Identify the preparation type.
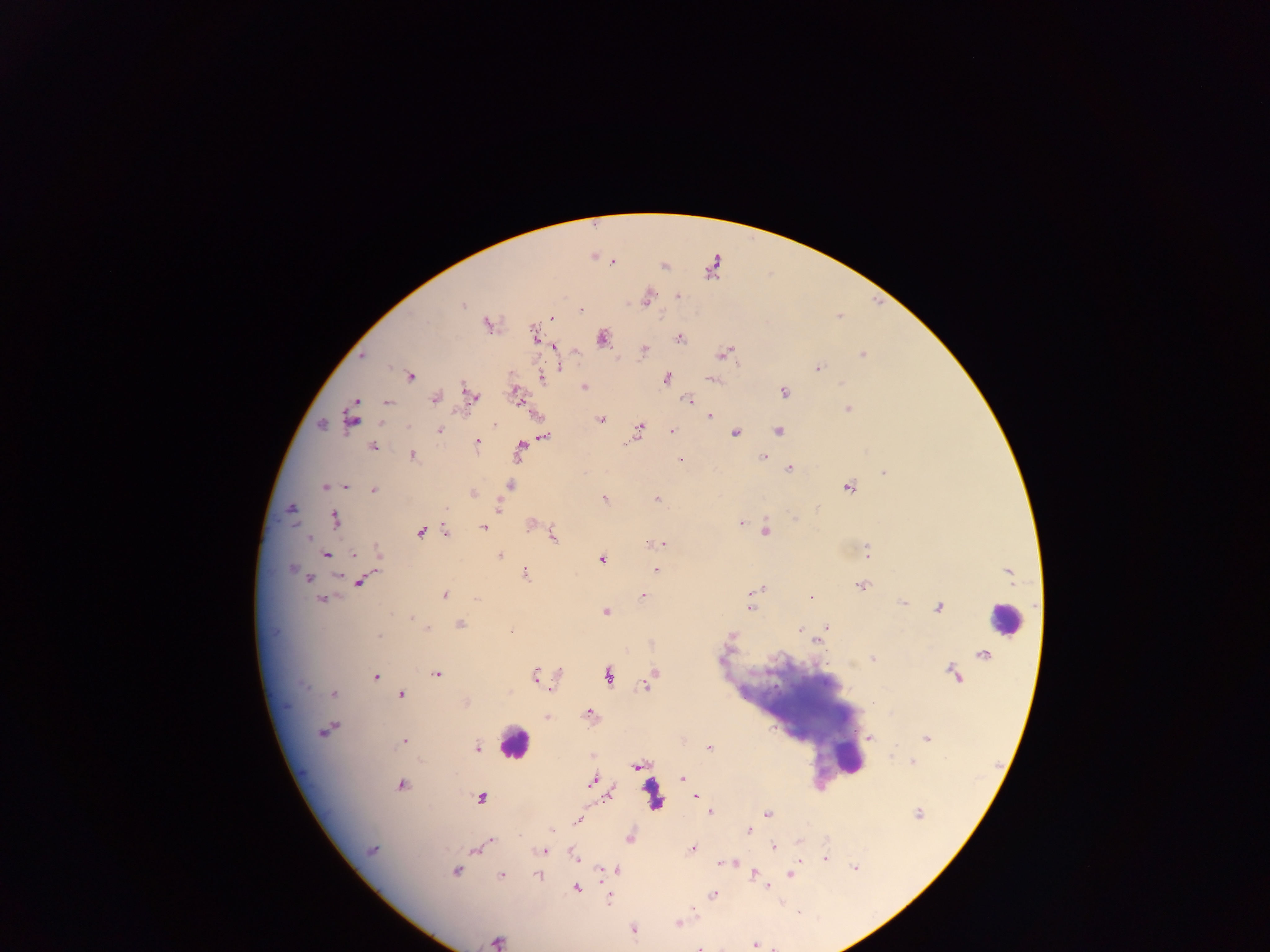
This is a thick smear.

capture = mobile-phone photograph through a microscope
leukocyte locations = approximate centers as [x, y] in pixels: [1004, 619], [513, 742], [849, 759], [652, 794]
image size = 1270×952 pixels
field of view = single
country = Ghana
malaria parasite locations = approximate centers as [x, y] in pixels: [592, 257], [613, 261], [664, 264], [677, 296], [647, 297], [462, 305], [581, 311], [551, 319], [488, 323], [534, 334], [603, 337], [679, 338], [554, 346], [644, 349], [724, 353], [862, 354], [362, 356], [560, 365], [817, 368], [409, 376], [540, 377], [666, 378], [712, 378], [584, 386], [783, 392], [515, 395], [472, 396], [434, 397], [687, 399], [519, 400], [355, 401], [386, 403], [847, 407], [710, 416], [352, 418], [601, 419], [495, 423], [320, 424], [639, 428], [777, 430], [440, 431], [671, 431], [735, 432], [542, 436], [477, 442], [372, 446], [519, 451], [412, 455], [762, 456], [679, 459], [789, 468], [884, 472], [509, 485], [324, 486], [346, 487], [848, 487], [373, 490], [471, 493], [604, 498], [656, 498], [497, 505], [290, 508], [335, 519], [797, 519], [530, 523], [740, 523], [483, 527], [765, 530], [420, 532], [445, 532], [552, 535], [306, 536], [659, 544], [378, 553], [866, 553], [326, 554], [499, 555], [353, 556], [601, 559], [291, 568], [655, 570], [1009, 571], [525, 573], [308, 578], [360, 581], [861, 585], [757, 591], [642, 595], [444, 596], [812, 598], [321, 599], [902, 603], [749, 607], [939, 607], [605, 612], [410, 615], [459, 624], [826, 626], [799, 628], [425, 629], [732, 635], [377, 637], [818, 638], [982, 655], [872, 658], [558, 672], [653, 673], [437, 674], [953, 674], [375, 676], [534, 676], [608, 676], [646, 685], [334, 693], [401, 695], [465, 703], [590, 715], [548, 717], [325, 730], [870, 738], [926, 738], [403, 741], [476, 747], [709, 748], [591, 756], [912, 761], [637, 764], [682, 778], [593, 780], [400, 785], [607, 795], [695, 796], [480, 798], [710, 811], [766, 814], [918, 814], [578, 819], [551, 829], [748, 831], [628, 838], [491, 839], [799, 843], [773, 847], [692, 849], [372, 850], [474, 850], [543, 850], [573, 854], [825, 858], [722, 862], [733, 863], [853, 868], [454, 870], [616, 870], [601, 871], [752, 873], [791, 874], [501, 875], [538, 875], [764, 885], [575, 887], [713, 894], [609, 895], [677, 923], [632, 929], [495, 942], [755, 945], [699, 946]